Report the malaria status of this cell.
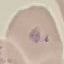
It is parasitized.

Automatically extracted cell patch, resized to 64 × 64 pixels. Giemsa stain. Thin blood film. Acquired by smartphone through the microscope eyepiece.